Describe the morphology of the erythrocytes.
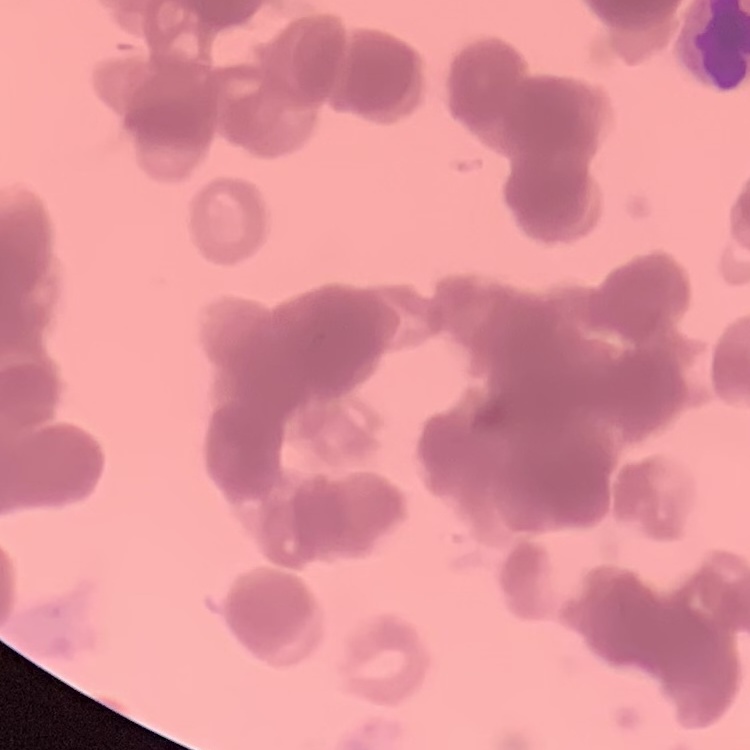

They show rouleaux formation.

One tile cut from a larger photomicrograph. Thin blood smear. Field's or Giemsa stain.